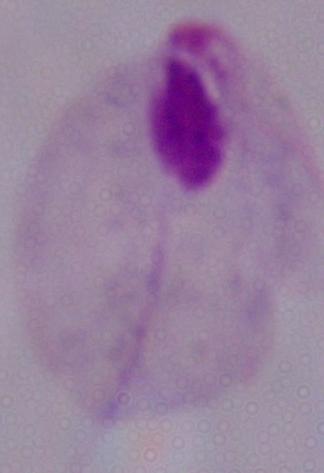

magnification = 1000x
modality = photomicrograph
identification = trichomonad